Assess for malaria.
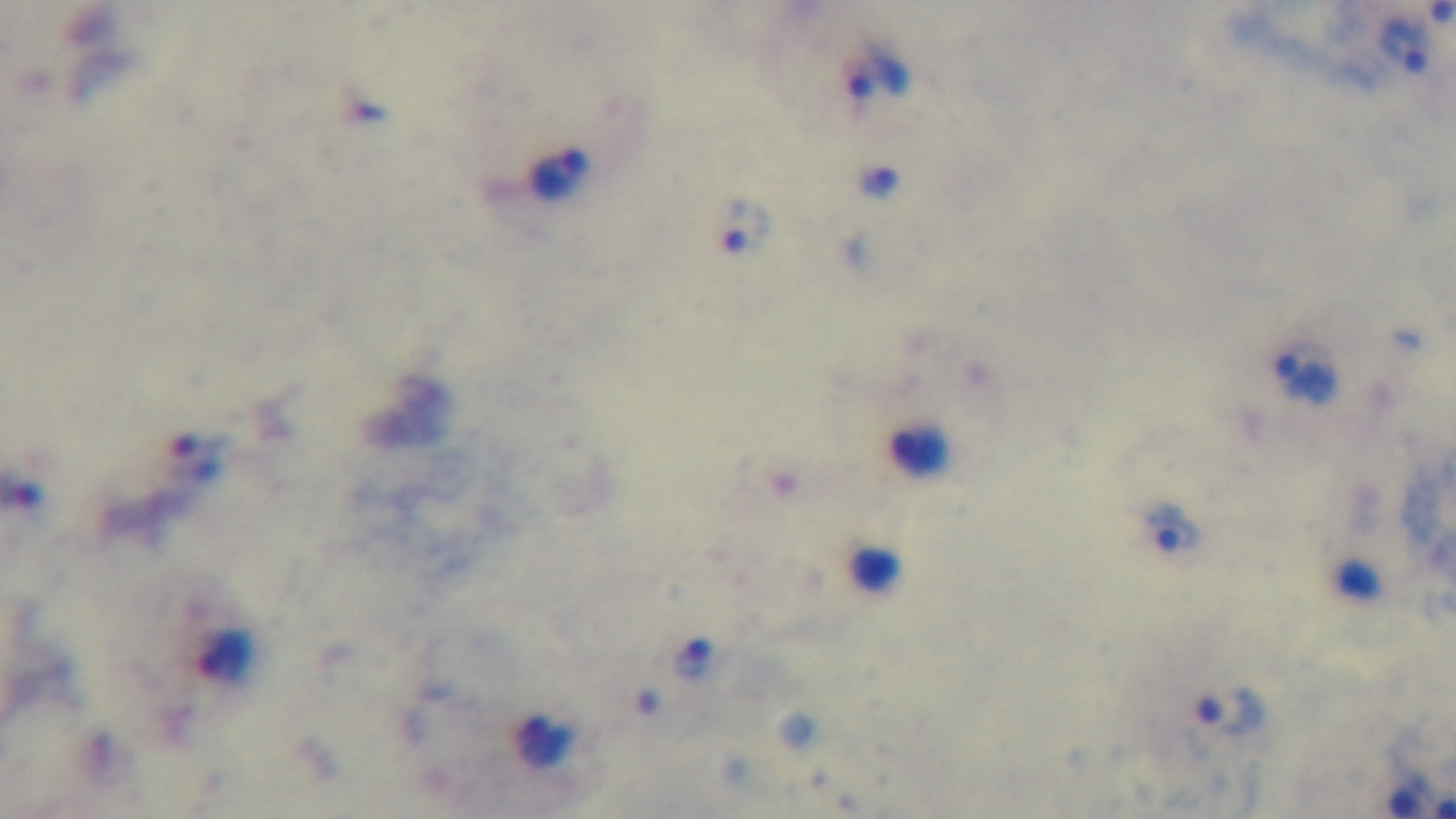
Infected.

stain = Giemsa
modality = light microscopy
field of view = single
capture = mounted 4K digital camera
objective = 100x oil immersion
preparation = thick